Assess this cell for malaria.
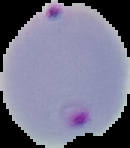
Parasitized.

Summary:
  - Image size: 130×148 pixels
  - Image type: cell region segmented out of the field of view; surrounding area masked to black
  - Preparation: thin blood film